Identify the blood parasite species.
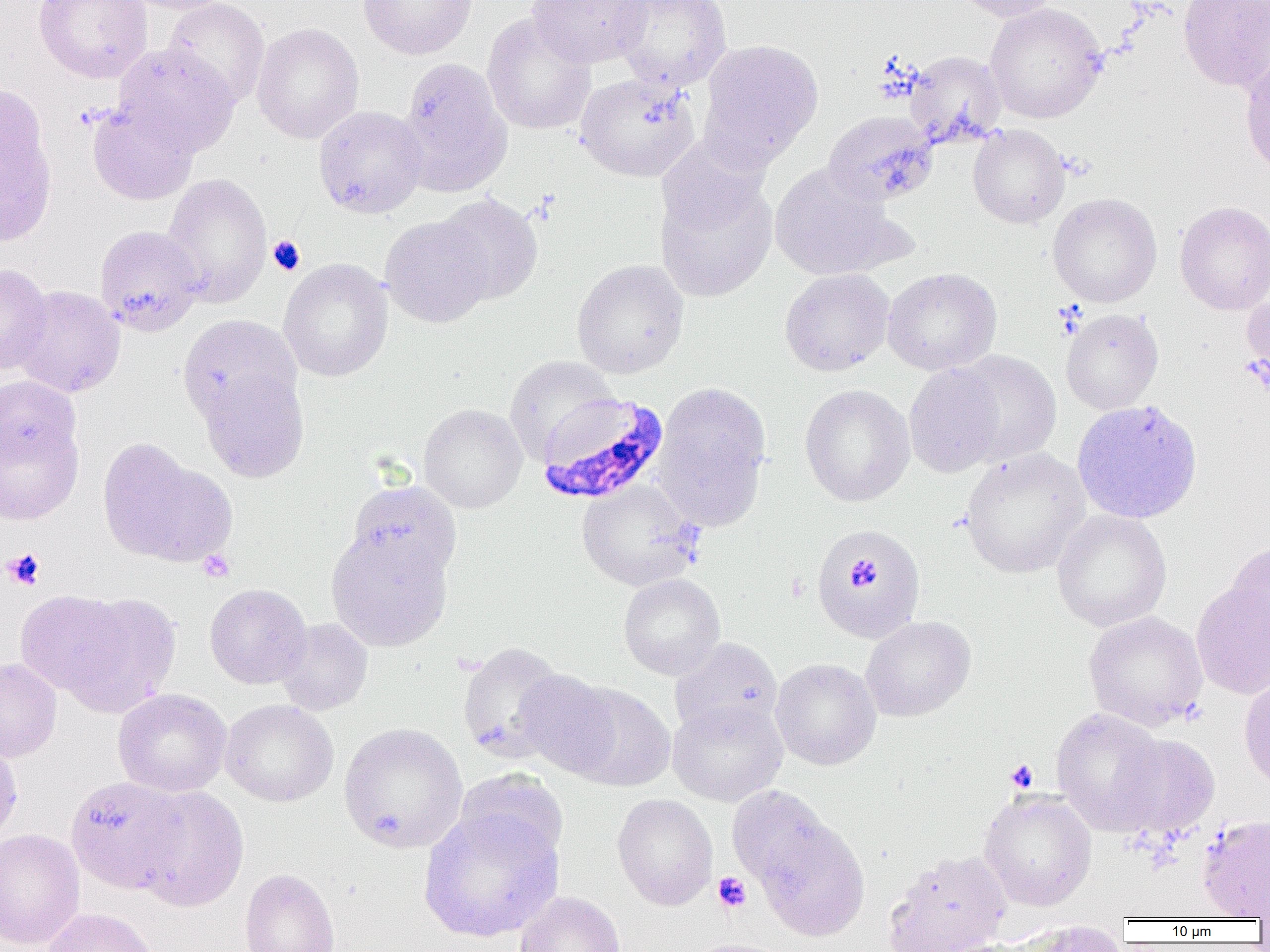
Plasmodium falciparum.

Approximate bounding boxes as named x1/y1/x2/y2 corners in pixels. Platelet locations: (x1=267, y1=236, x2=305, y2=275), (x1=3, y1=547, x2=45, y2=590), (x1=198, y1=549, x2=235, y2=583), (x1=852, y1=563, x2=879, y2=587), (x1=1006, y1=760, x2=1038, y2=792), (x1=713, y1=872, x2=752, y2=912). Uninfected red blood cell locations: (x1=34, y1=0, x2=153, y2=83), (x1=120, y1=0, x2=234, y2=15), (x1=163, y1=0, x2=270, y2=107), (x1=357, y1=0, x2=478, y2=60), (x1=527, y1=0, x2=650, y2=69), (x1=613, y1=0, x2=732, y2=91), (x1=952, y1=0, x2=1062, y2=22), (x1=1177, y1=0, x2=1270, y2=92), (x1=984, y1=2, x2=1108, y2=123), (x1=482, y1=14, x2=597, y2=135), (x1=252, y1=22, x2=364, y2=144), (x1=697, y1=38, x2=824, y2=170), (x1=114, y1=44, x2=239, y2=156), (x1=1239, y1=44, x2=1270, y2=180), (x1=905, y1=50, x2=1007, y2=148), (x1=398, y1=57, x2=511, y2=194), (x1=575, y1=71, x2=700, y2=182), (x1=0, y1=83, x2=58, y2=249), (x1=86, y1=101, x2=199, y2=206), (x1=313, y1=105, x2=428, y2=218), (x1=823, y1=110, x2=939, y2=206), (x1=968, y1=124, x2=1070, y2=229), (x1=770, y1=164, x2=903, y2=281), (x1=654, y1=168, x2=778, y2=302), (x1=162, y1=173, x2=272, y2=307), (x1=1047, y1=192, x2=1162, y2=308), (x1=436, y1=194, x2=543, y2=304), (x1=1174, y1=200, x2=1270, y2=315), (x1=379, y1=214, x2=495, y2=328), (x1=95, y1=225, x2=204, y2=336), (x1=278, y1=258, x2=393, y2=382), (x1=571, y1=259, x2=689, y2=379), (x1=0, y1=263, x2=52, y2=374), (x1=882, y1=267, x2=1002, y2=375), (x1=779, y1=268, x2=894, y2=376), (x1=1241, y1=284, x2=1270, y2=395), (x1=10, y1=285, x2=126, y2=397), (x1=1061, y1=308, x2=1164, y2=415), (x1=177, y1=314, x2=301, y2=426), (x1=948, y1=349, x2=1062, y2=467), (x1=504, y1=355, x2=618, y2=463), (x1=904, y1=363, x2=1007, y2=478), (x1=200, y1=369, x2=309, y2=483), (x1=0, y1=375, x2=81, y2=469), (x1=652, y1=381, x2=772, y2=530), (x1=799, y1=383, x2=915, y2=506), (x1=1071, y1=399, x2=1203, y2=524), (x1=418, y1=403, x2=528, y2=513), (x1=0, y1=416, x2=84, y2=524), (x1=97, y1=439, x2=235, y2=569), (x1=960, y1=448, x2=1091, y2=578), (x1=576, y1=479, x2=702, y2=591), (x1=345, y1=480, x2=462, y2=586), (x1=1051, y1=509, x2=1171, y2=632), (x1=811, y1=523, x2=926, y2=644), (x1=326, y1=529, x2=453, y2=650), (x1=1226, y1=541, x2=1270, y2=653), (x1=618, y1=573, x2=726, y2=680), (x1=1191, y1=580, x2=1270, y2=699), (x1=204, y1=583, x2=312, y2=689), (x1=14, y1=590, x2=133, y2=697), (x1=55, y1=592, x2=182, y2=718), (x1=1083, y1=611, x2=1208, y2=730), (x1=861, y1=615, x2=976, y2=722), (x1=274, y1=618, x2=373, y2=715), (x1=670, y1=638, x2=783, y2=739), (x1=457, y1=642, x2=568, y2=763), (x1=0, y1=657, x2=62, y2=762), (x1=771, y1=658, x2=881, y2=770), (x1=514, y1=670, x2=622, y2=779), (x1=1239, y1=675, x2=1270, y2=792), (x1=563, y1=682, x2=676, y2=791), (x1=113, y1=688, x2=232, y2=797), (x1=220, y1=699, x2=338, y2=806), (x1=667, y1=699, x2=788, y2=806), (x1=1051, y1=708, x2=1170, y2=835), (x1=338, y1=723, x2=468, y2=853), (x1=1113, y1=734, x2=1220, y2=840), (x1=0, y1=736, x2=22, y2=845), (x1=454, y1=769, x2=569, y2=868), (x1=65, y1=776, x2=188, y2=893), (x1=131, y1=785, x2=249, y2=911), (x1=726, y1=785, x2=835, y2=890), (x1=979, y1=789, x2=1097, y2=911), (x1=612, y1=793, x2=718, y2=910), (x1=418, y1=809, x2=563, y2=942), (x1=1197, y1=815, x2=1270, y2=919), (x1=756, y1=819, x2=870, y2=942), (x1=0, y1=829, x2=86, y2=949), (x1=883, y1=850, x2=1012, y2=952), (x1=239, y1=868, x2=340, y2=952), (x1=514, y1=891, x2=626, y2=952), (x1=41, y1=907, x2=160, y2=952), (x1=1011, y1=920, x2=1129, y2=952), (x1=683, y1=938, x2=794, y2=952), (x1=932, y1=938, x2=1042, y2=952). Plasmodium falciparum-infected red blood cell locations: (x1=535, y1=392, x2=669, y2=505). 1000x magnification. Light microscopy. One field of a larger specimen. Image is 1270×952 pixels. Thin blood film.